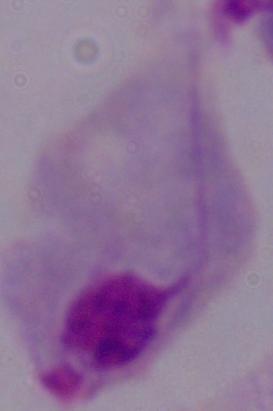
Summary:
  - Modality: micrograph
  - Identification: trichomonad
  - Magnification: 1000x